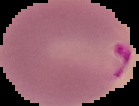

Summary:
  - Preparation: thin blood smear
  - Result: Plasmodium parasites identified
  - Image type: segmented cell region with the area outside set to black
  - Image size: 139×106 pixels